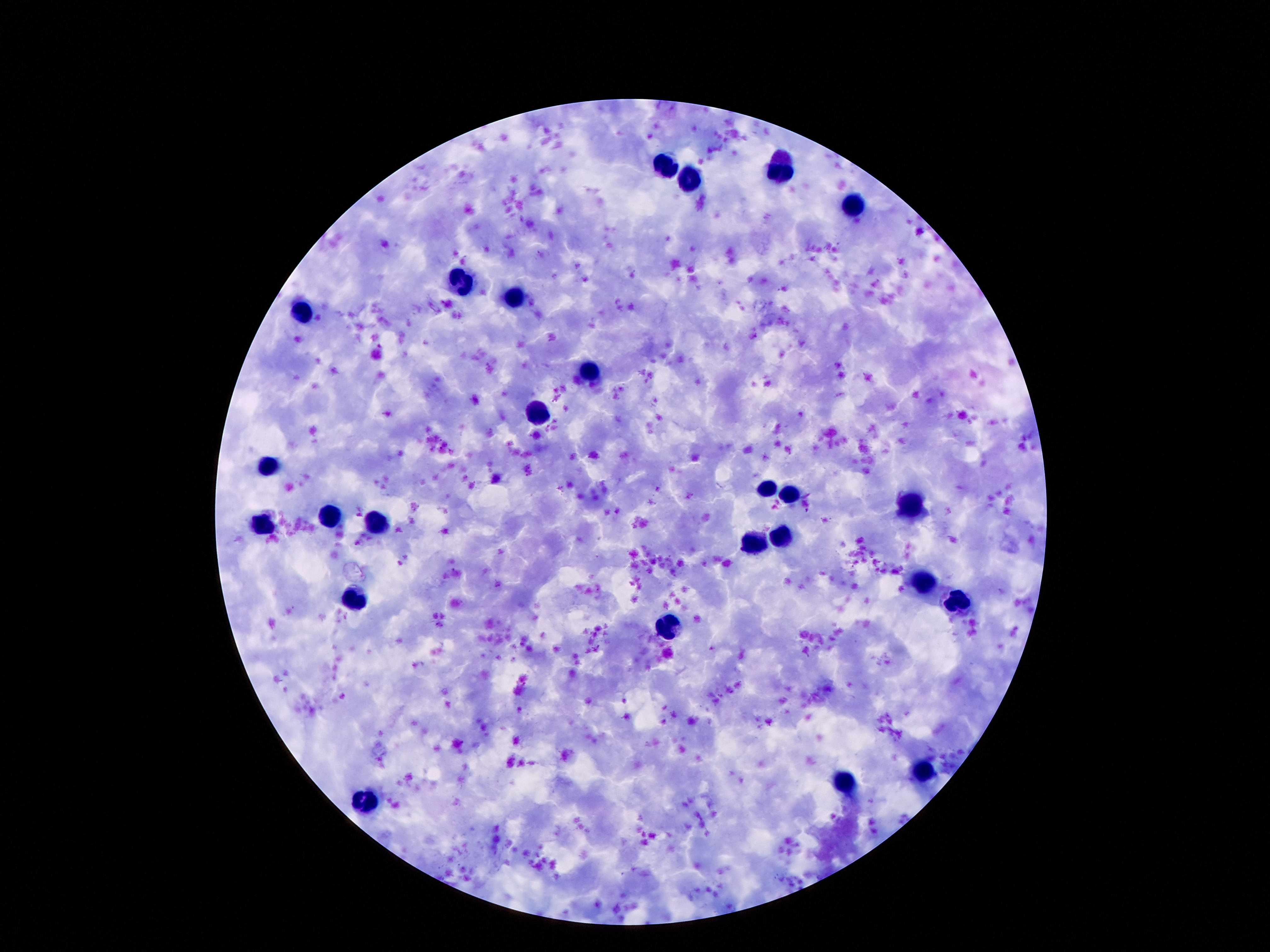
Approximate centers as (x, y) in pixels.
Summary:
  - Leukocyte locations: (665, 164), (779, 170), (690, 178), (852, 206), (457, 284), (514, 295), (302, 312), (585, 373), (539, 416), (268, 466), (769, 488), (792, 492), (910, 508), (332, 515), (375, 525), (262, 526), (785, 537), (753, 543), (925, 584), (359, 597), (960, 603), (666, 626), (926, 772), (845, 781), (365, 802)
  - Field of view: single
  - Capture: smartphone camera through the microscope eyepiece
  - Patient malaria status: not infected
  - Preparation: thick blood smear
  - Stain: Giemsa
  - Image size: 1270×952 pixels
  - Magnification: 100x